Comment on the morphology of the erythrocytes.
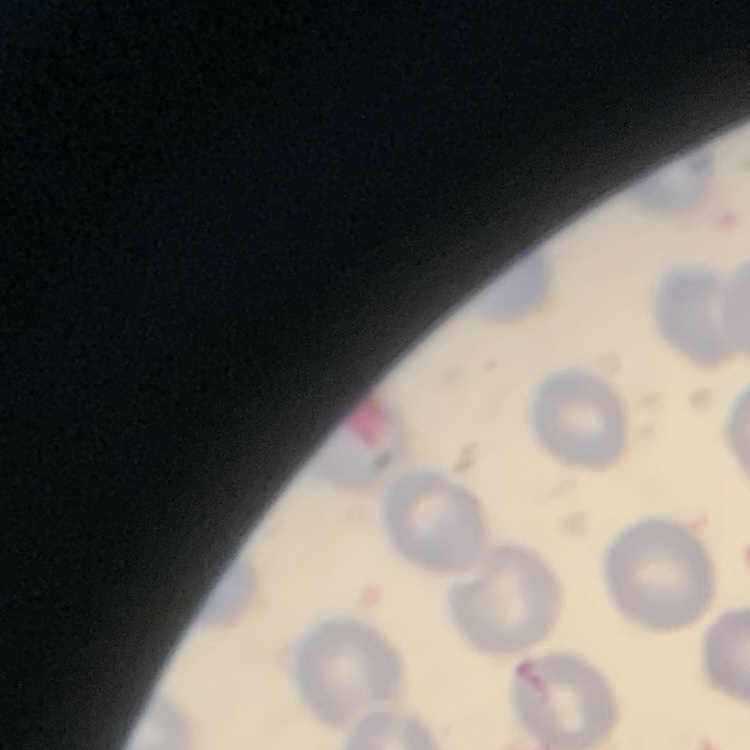
No rouleaux formation.

Stained with either Field's or Giemsa. Square crop of a larger photomicrograph. Thin blood smear.